Point out each malaria parasite.
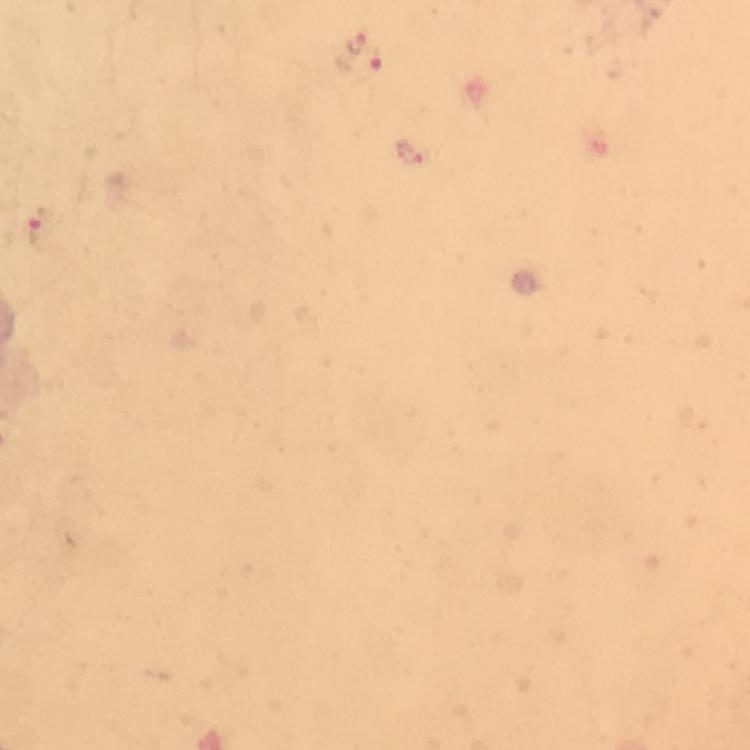
Approximate centers as {x, y} in pixels.
Malaria parasites: {356, 41}, {375, 60}, {410, 153}, {42, 228}.

Photographed through the microscope with a smartphone camera. At 100x magnification. Image is 750×750 pixels. A crop from one field of view. Immersion oil was used. From a diagnostic examination for malaria. Thick smear. Giemsa-stained preparation.